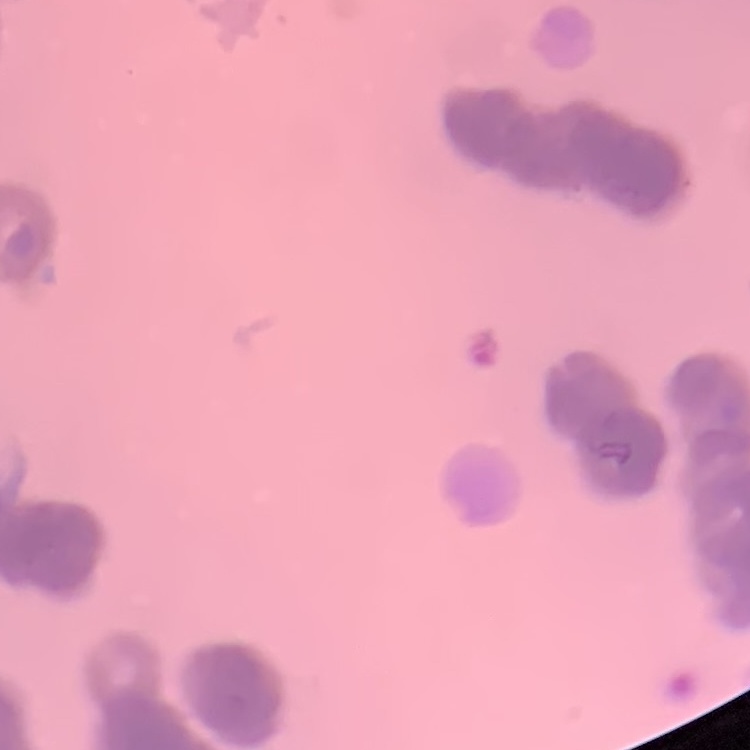
The erythrocytes show rouleaux formation. Thin peripheral smear. One tile cut from a larger photomicrograph. Field's or Giemsa stain.